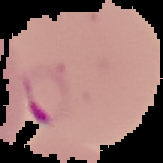
Cell region segmented out of the field of view; the surrounding area is masked to black. Image is 163×163 pixels. Result: malaria parasites identified. From a thin blood film.